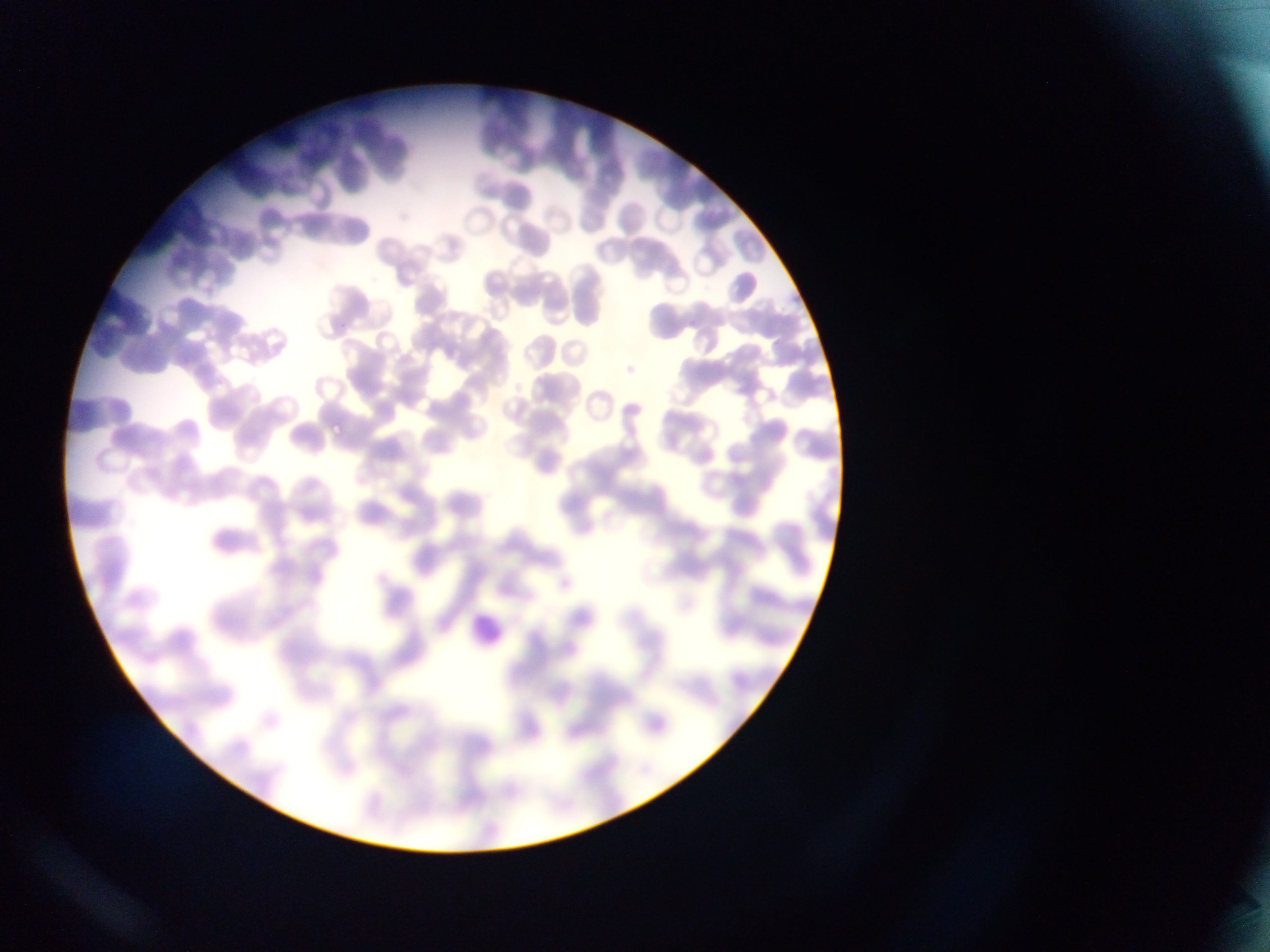
Approximate bounding boxes as {left, top, right, bottom} in pixels. Leukocyte locations: {460, 606, 504, 656}. Malaria parasite locations: {689, 319, 700, 327}, {338, 321, 351, 331}, {329, 419, 346, 434}. Single field of view. Photographed through a microscope with a mobile-phone camera. Image is 1270×952 pixels. Sample from Ghana. Thin blood smear.